Outline each blood parasite and name the species.
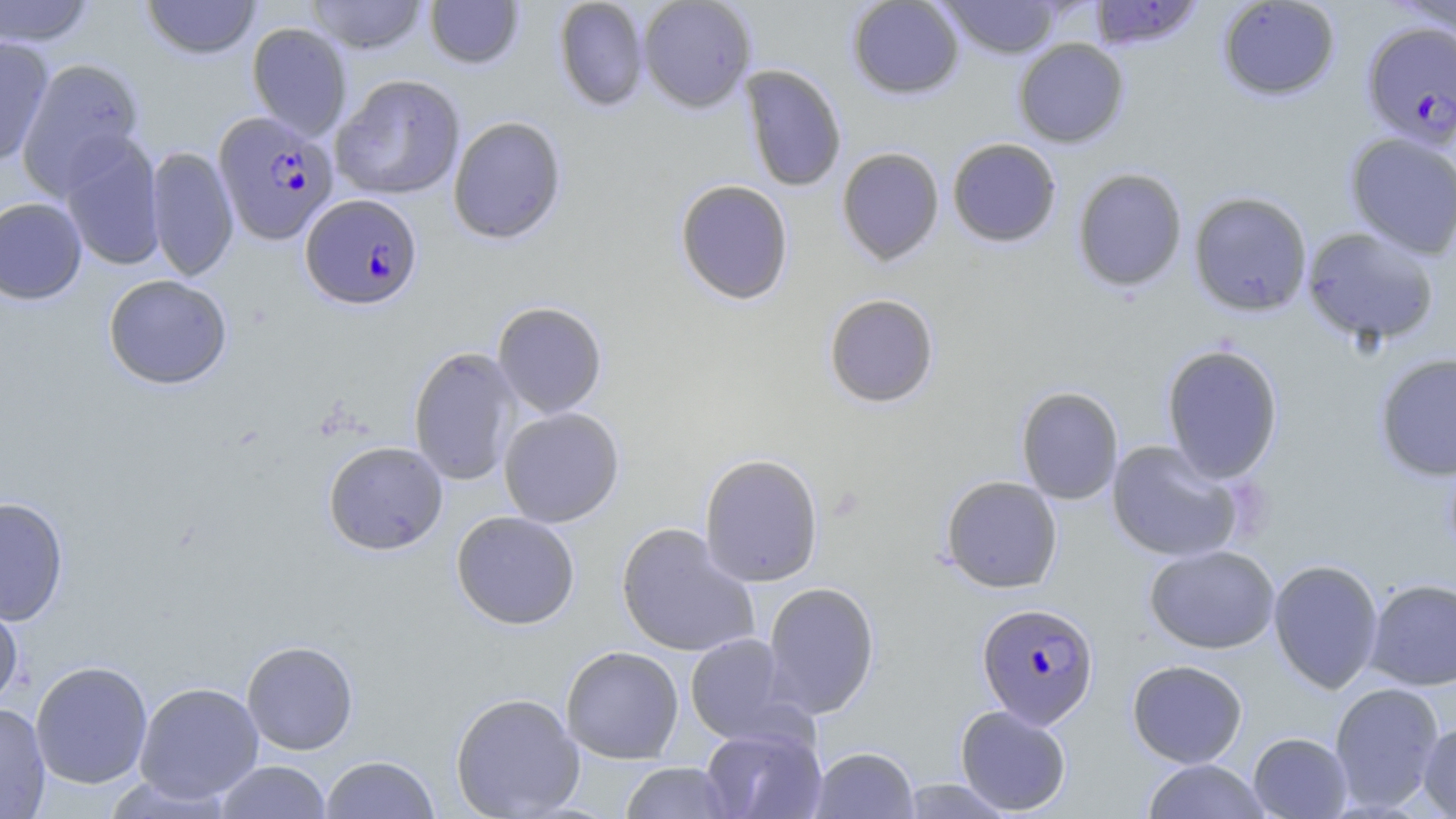
Approximate bounding boxes as named x1/y1/x2/y2 corners in pixels.
Plasmodium falciparum-infected red blood cells: (x1=1361, y1=21, x2=1456, y2=149), (x1=214, y1=111, x2=338, y2=246), (x1=300, y1=193, x2=423, y2=310), (x1=976, y1=602, x2=1100, y2=728).
No Plasmodium ovale, Plasmodium malariae, Plasmodium vivax, Babesia divergens, or Trypanosoma brucei observed.

Uninfected red blood cell locations: (x1=0, y1=0, x2=98, y2=47), (x1=141, y1=0, x2=262, y2=60), (x1=306, y1=0, x2=428, y2=54), (x1=423, y1=0, x2=525, y2=70), (x1=553, y1=0, x2=650, y2=112), (x1=637, y1=0, x2=757, y2=113), (x1=846, y1=0, x2=965, y2=100), (x1=939, y1=0, x2=1064, y2=59), (x1=1216, y1=0, x2=1341, y2=101), (x1=1390, y1=0, x2=1456, y2=44), (x1=1088, y1=1, x2=1204, y2=50), (x1=246, y1=22, x2=352, y2=140), (x1=0, y1=35, x2=54, y2=167), (x1=1013, y1=38, x2=1129, y2=148), (x1=16, y1=57, x2=145, y2=196), (x1=740, y1=65, x2=847, y2=192), (x1=331, y1=74, x2=466, y2=200), (x1=448, y1=115, x2=567, y2=244), (x1=1344, y1=132, x2=1456, y2=258), (x1=58, y1=133, x2=165, y2=272), (x1=946, y1=138, x2=1062, y2=248), (x1=146, y1=146, x2=239, y2=281), (x1=836, y1=147, x2=945, y2=266), (x1=1072, y1=167, x2=1188, y2=293), (x1=674, y1=179, x2=794, y2=305), (x1=1188, y1=191, x2=1313, y2=316), (x1=0, y1=197, x2=88, y2=304), (x1=1301, y1=226, x2=1440, y2=348), (x1=103, y1=274, x2=233, y2=389), (x1=823, y1=293, x2=940, y2=408), (x1=492, y1=301, x2=607, y2=418), (x1=1161, y1=344, x2=1284, y2=483), (x1=408, y1=346, x2=522, y2=486), (x1=1374, y1=353, x2=1456, y2=481), (x1=1015, y1=385, x2=1124, y2=505), (x1=498, y1=407, x2=625, y2=527), (x1=323, y1=440, x2=448, y2=555), (x1=1106, y1=440, x2=1244, y2=562), (x1=699, y1=453, x2=824, y2=587), (x1=940, y1=475, x2=1063, y2=594), (x1=0, y1=496, x2=69, y2=626), (x1=451, y1=510, x2=580, y2=630), (x1=616, y1=522, x2=760, y2=658), (x1=1144, y1=544, x2=1280, y2=654), (x1=1268, y1=559, x2=1384, y2=694), (x1=1365, y1=578, x2=1456, y2=690), (x1=762, y1=581, x2=880, y2=718), (x1=0, y1=593, x2=24, y2=711), (x1=685, y1=633, x2=798, y2=745), (x1=242, y1=640, x2=358, y2=755), (x1=561, y1=646, x2=684, y2=764), (x1=1126, y1=659, x2=1248, y2=768), (x1=30, y1=660, x2=153, y2=789), (x1=134, y1=681, x2=264, y2=803), (x1=1329, y1=682, x2=1445, y2=811), (x1=450, y1=692, x2=585, y2=819), (x1=0, y1=701, x2=51, y2=818), (x1=955, y1=705, x2=1072, y2=815), (x1=1418, y1=720, x2=1456, y2=818), (x1=700, y1=725, x2=827, y2=819), (x1=1248, y1=732, x2=1353, y2=818), (x1=810, y1=746, x2=919, y2=819), (x1=320, y1=755, x2=439, y2=819), (x1=1142, y1=759, x2=1270, y2=818), (x1=213, y1=760, x2=331, y2=819), (x1=620, y1=762, x2=734, y2=819), (x1=899, y1=778, x2=1016, y2=818). Slide-level diagnosis: Plasmodium falciparum. Captured at 1000x magnification. Light microscopy. Thin blood film. Image is 1456×819 pixels. May-Grünwald-Giemsa-stained preparation. One field of a larger specimen.